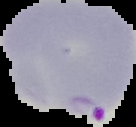
{
  "preparation": "thin blood smear",
  "image_size": "136×127 pixels",
  "image_type": "cell region segmented out of the field of view; surrounding area masked to black",
  "result": "Plasmodium parasites identified"
}